Classify this cell by malaria status.
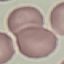

Uninfected.

Thin blood film. Automatically extracted cell patch, resized to 64 × 64 pixels. Giemsa stain. Photographed with a smartphone camera at the microscope eyepiece.